Classify this cell by malaria status.
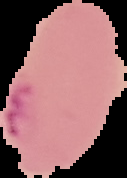
Parasitized.

Image is 127×178 pixels. From a thin blood film. Segmented cell region on a black background.